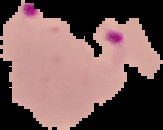 Malaria status: parasitized. From a thin blood smear. Segmented cell region on a black background. Image is 163×130 pixels.